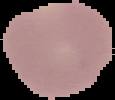

Summary:
  - Image type: segmented cell region with the area outside set to black
  - Image size: 115×100 pixels
  - Malaria status: parasitized
  - Preparation: thin blood smear